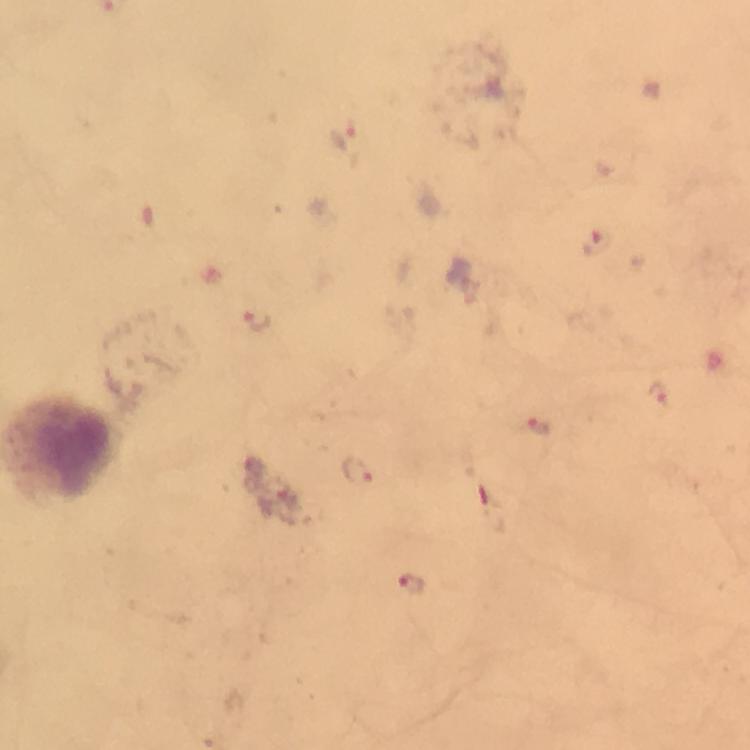

Approximate object centers, in pixels from the top-left corner.
Summary:
  - Plasmodium parasite locations: (x=344, y=137), (x=596, y=245), (x=257, y=321), (x=658, y=394), (x=536, y=426), (x=355, y=471), (x=411, y=585)
  - Capture: smartphone camera through the microscope
  - Image size: 750×750 pixels
  - Context: from a malaria diagnostic workup
  - Preparation: thick blood smear
  - Magnification: 100x
  - Stain: Giemsa
  - Immersion oil: used
  - Cropped from: a single field of view